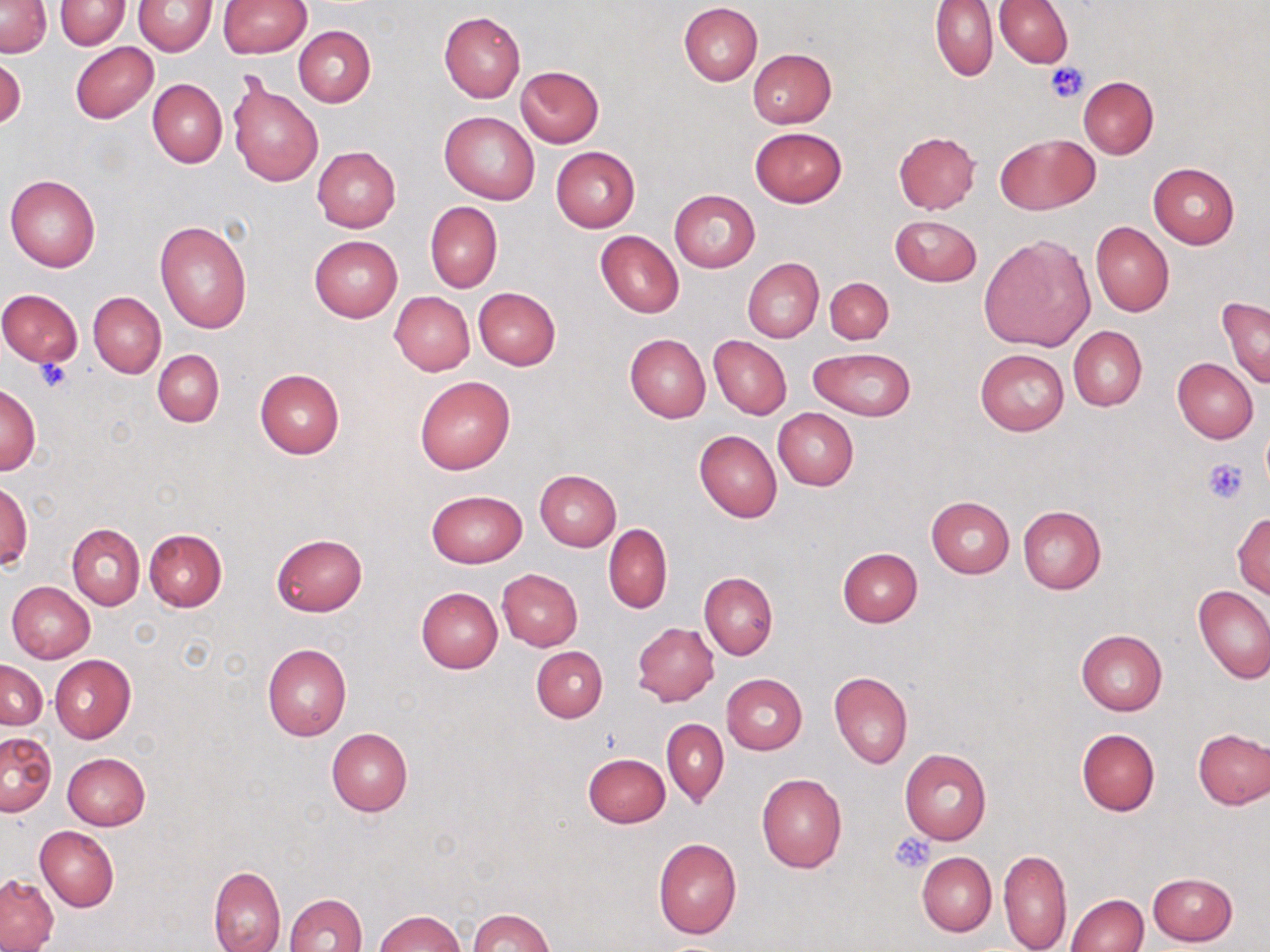
Summary:
  - Coordinate format: approximate bounding boxes as [x1, y1, x2, y2] in pixels
  - Platelet locations: [1046, 62, 1088, 102], [36, 359, 71, 392], [1203, 457, 1250, 506], [890, 831, 934, 874]
  - Uninfected red blood cell locations: [931, 0, 998, 80], [0, 1, 51, 57], [55, 1, 129, 50], [133, 1, 218, 56], [219, 1, 311, 57], [995, 1, 1072, 68], [678, 2, 763, 85], [438, 11, 525, 102], [293, 26, 376, 106], [70, 42, 158, 123], [747, 49, 837, 128], [515, 66, 604, 147], [1078, 76, 1159, 159], [228, 78, 324, 187], [147, 79, 226, 167], [439, 112, 540, 203], [749, 126, 848, 208], [893, 130, 981, 213], [995, 134, 1096, 215], [550, 146, 640, 232], [312, 147, 400, 233], [1148, 163, 1239, 248], [5, 174, 101, 273], [669, 189, 760, 273], [425, 202, 503, 293], [890, 214, 982, 286], [155, 221, 251, 334], [1090, 221, 1173, 316], [596, 230, 683, 317], [980, 234, 1094, 352], [308, 235, 402, 322], [742, 258, 823, 343], [824, 276, 894, 344], [473, 287, 561, 369], [0, 288, 82, 369], [390, 291, 475, 375], [89, 292, 165, 377], [1218, 296, 1270, 388], [1069, 326, 1146, 411], [624, 334, 711, 422], [709, 336, 792, 418], [807, 347, 917, 421], [975, 348, 1069, 435], [152, 349, 224, 426], [1173, 357, 1258, 444], [255, 369, 345, 458], [414, 375, 516, 475], [0, 382, 41, 475], [773, 408, 859, 489], [694, 430, 782, 522], [534, 470, 620, 552], [1, 481, 32, 571], [426, 490, 527, 567], [926, 496, 1015, 578], [1017, 506, 1106, 594], [1233, 512, 1270, 597], [67, 523, 144, 610], [603, 524, 672, 613], [144, 528, 227, 611], [270, 533, 367, 617], [836, 548, 922, 628], [498, 568, 583, 651], [699, 572, 778, 659], [6, 582, 94, 663], [1193, 585, 1270, 684], [415, 588, 502, 673], [632, 622, 718, 706], [1076, 629, 1167, 714], [262, 644, 351, 741], [532, 646, 606, 722], [50, 655, 136, 744], [1, 658, 47, 730], [828, 671, 912, 769], [722, 673, 807, 755], [663, 718, 729, 807], [326, 727, 413, 816], [1076, 727, 1160, 816], [1194, 727, 1270, 809], [0, 732, 56, 816], [900, 749, 992, 845], [62, 752, 150, 829], [582, 752, 670, 827], [757, 773, 847, 873], [35, 826, 119, 912], [653, 838, 742, 940], [998, 849, 1072, 952], [917, 851, 996, 937], [208, 865, 285, 952], [1147, 872, 1237, 946], [0, 874, 58, 951], [284, 892, 367, 952], [1067, 893, 1147, 952], [469, 908, 552, 952], [373, 911, 467, 952]
  - Slide-level diagnosis: negative for blood parasites
  - Magnification: 1000x
  - Image size: 1270×952 pixels
  - Stain: May-Grünwald-Giemsa
  - Field of view: one of a larger specimen
  - Modality: optical microscopy
  - Preparation: thin blood film